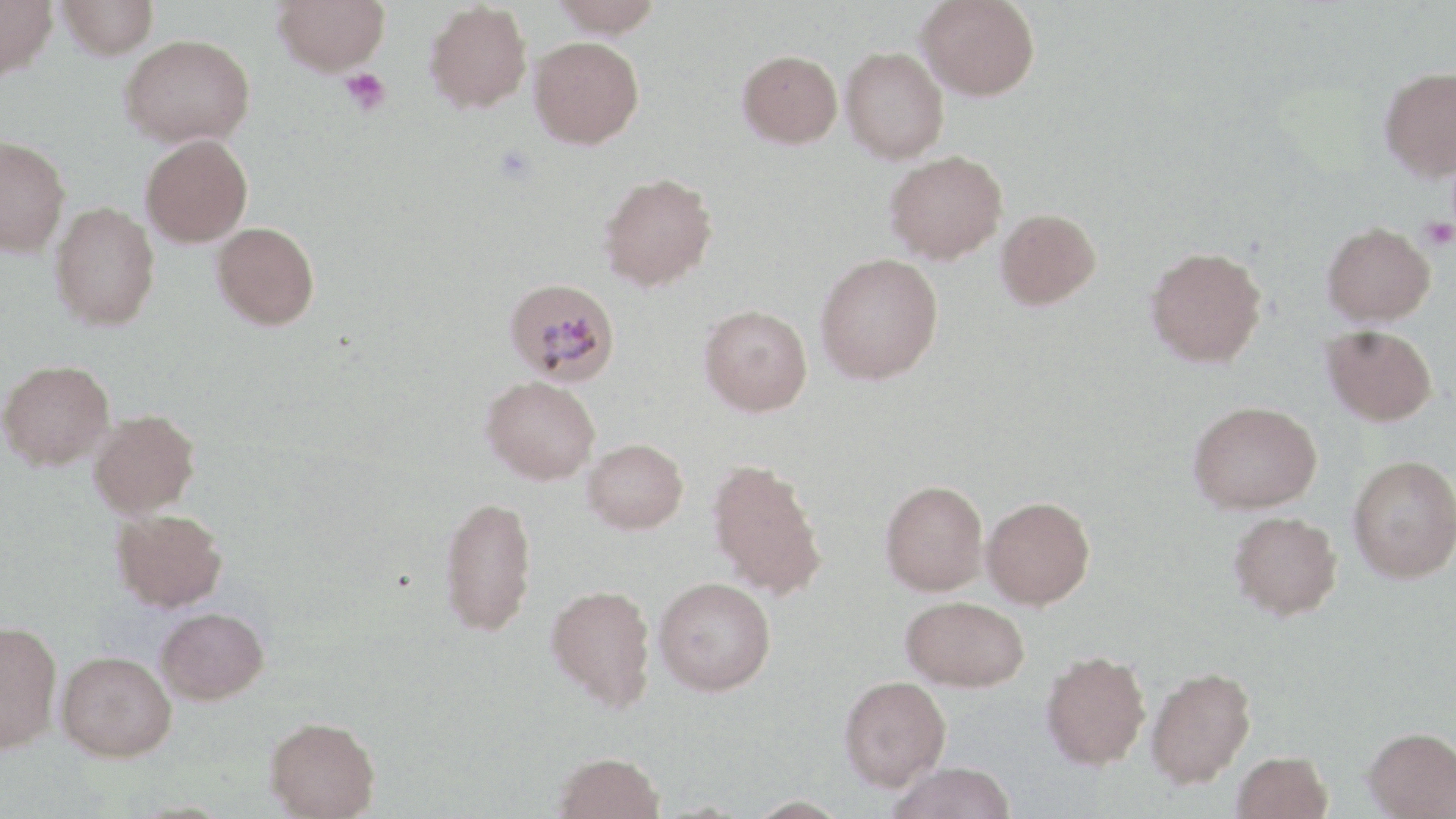 Approximate bounding boxes as (x1,y1)-(x2,y2) corner pairs in pixels. Plasmodium malariae-infected red blood cell locations: (504,278)-(620,386). Platelet locations: (340,68)-(391,116), (1421,217)-(1456,251). Uninfected red blood cell locations: (0,0)-(58,80), (57,0)-(159,59), (274,0)-(389,76), (550,0)-(666,37), (917,0)-(1040,101), (424,1)-(533,113), (119,33)-(256,147), (529,36)-(644,149), (841,47)-(947,162), (737,49)-(843,148), (1379,66)-(1456,181), (140,134)-(253,247), (0,136)-(70,257), (884,150)-(1008,264), (599,171)-(718,291), (49,202)-(160,331), (995,208)-(1101,310), (212,221)-(319,330), (1321,222)-(1435,326), (1145,246)-(1267,368), (815,252)-(943,384), (699,304)-(812,416), (1322,325)-(1437,426), (0,359)-(114,471), (482,376)-(600,484), (1188,400)-(1322,514), (89,410)-(200,518), (582,438)-(688,534), (1348,454)-(1456,583), (706,457)-(827,599), (881,479)-(989,595), (439,495)-(537,635), (981,496)-(1095,609), (110,508)-(227,612), (1228,511)-(1342,620), (654,576)-(776,695), (546,583)-(656,711), (901,595)-(1029,692), (156,607)-(269,705), (0,620)-(61,753), (1041,649)-(1150,769), (56,650)-(177,761), (1146,667)-(1256,788), (839,675)-(951,789), (265,716)-(380,818), (1364,727)-(1456,818), (553,751)-(665,819), (1232,751)-(1333,819), (884,762)-(1017,819), (740,797)-(853,818). Slide-level diagnosis: Plasmodium malariae. Single field of view. Image is 1456×819 pixels. 1000x magnification. May-Grünwald-Giemsa-stained preparation. Light microscopy. Thin blood smear.